Assess this cell for malaria.
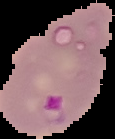
Parasitized.

Summary:
  - Image size: 115×139 pixels
  - Preparation: thin blood film
  - Image type: segmented cell region on a black background